Assess this cell for malaria.
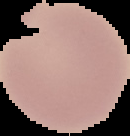
Uninfected.

Image is 130×136 pixels. Segmented cell region on a black background. From a thin blood smear.